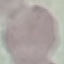

Summary:
  - Result: no malaria parasites detected
  - Stain: Giemsa
  - Image type: automatically extracted cell patch, resized to 64 × 64 pixels
  - Capture: smartphone through the microscope eyepiece
  - Preparation: thin blood film